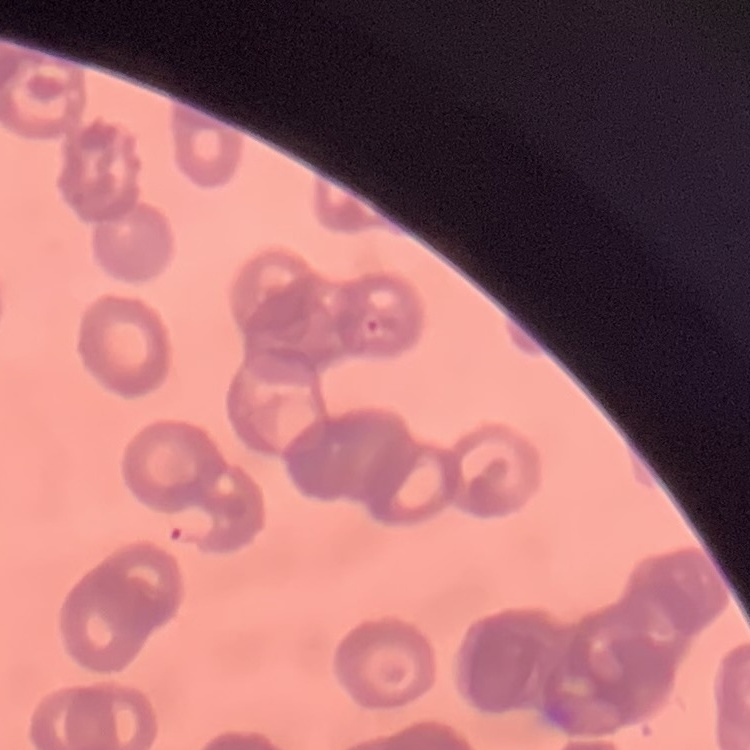
erythrocyte morphology = rouleaux formation
stain = Field's or Giemsa
image type = one tile cut from a larger photomicrograph
preparation = thin blood film